Locate and identify every blood parasite.
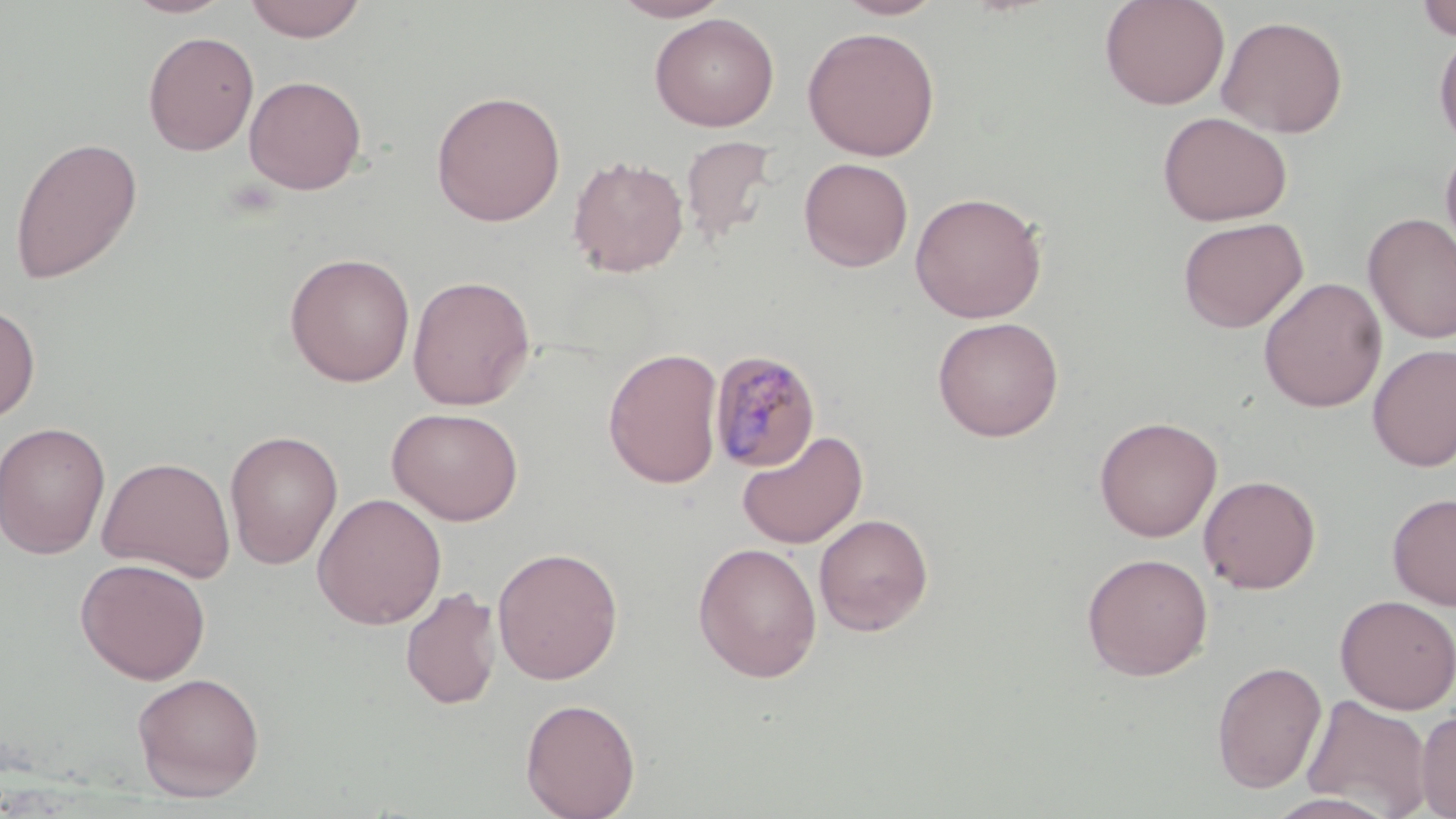
Approximate bounding boxes as [x1, y1, x2, y2] in pixels.
Plasmodium malariae-infected red blood cells: [707, 350, 821, 473].
No Plasmodium falciparum, Plasmodium ovale, Plasmodium vivax, Babesia divergens, or Trypanosoma brucei observed.

slide-level diagnosis = Plasmodium malariae
magnification = 1000x
modality = optical microscopy
field of view = one of a larger specimen
preparation = thin blood smear
image size = 1456×819 pixels
uninfected red blood cell locations = approximate bounding boxes as [x1, y1, x2, y2] in pixels: [123, 0, 235, 18], [244, 0, 367, 42], [611, 0, 732, 22], [832, 0, 947, 20], [1099, 0, 1230, 110], [1415, 0, 1456, 41], [649, 12, 780, 132], [1216, 14, 1349, 138], [802, 26, 941, 161], [1433, 29, 1456, 148], [143, 31, 259, 156], [243, 74, 367, 195], [430, 89, 566, 227], [1157, 110, 1293, 226], [8, 136, 143, 285], [680, 136, 780, 245], [1440, 138, 1456, 266], [568, 155, 690, 277], [798, 157, 914, 272], [909, 191, 1047, 324], [1362, 213, 1456, 344], [1177, 217, 1308, 333], [283, 252, 416, 387], [407, 274, 536, 410], [1258, 277, 1387, 412], [0, 301, 41, 423], [931, 316, 1064, 442], [1367, 344, 1456, 471], [603, 347, 724, 489], [387, 407, 524, 526], [1094, 416, 1222, 542], [0, 421, 111, 559], [224, 429, 343, 570], [736, 429, 868, 549], [97, 456, 236, 582], [1198, 474, 1321, 594], [311, 492, 447, 630], [1387, 492, 1456, 610], [813, 513, 934, 636], [693, 542, 823, 683], [491, 546, 624, 685], [1080, 552, 1214, 681], [75, 557, 211, 684], [400, 586, 501, 710], [1335, 594, 1456, 713], [1211, 660, 1327, 794], [131, 672, 266, 801], [1302, 695, 1434, 818], [520, 697, 641, 819], [1416, 708, 1456, 818], [1263, 793, 1398, 819]
stain = May-Grünwald-Giemsa